Locate every uninfected red blood cell.
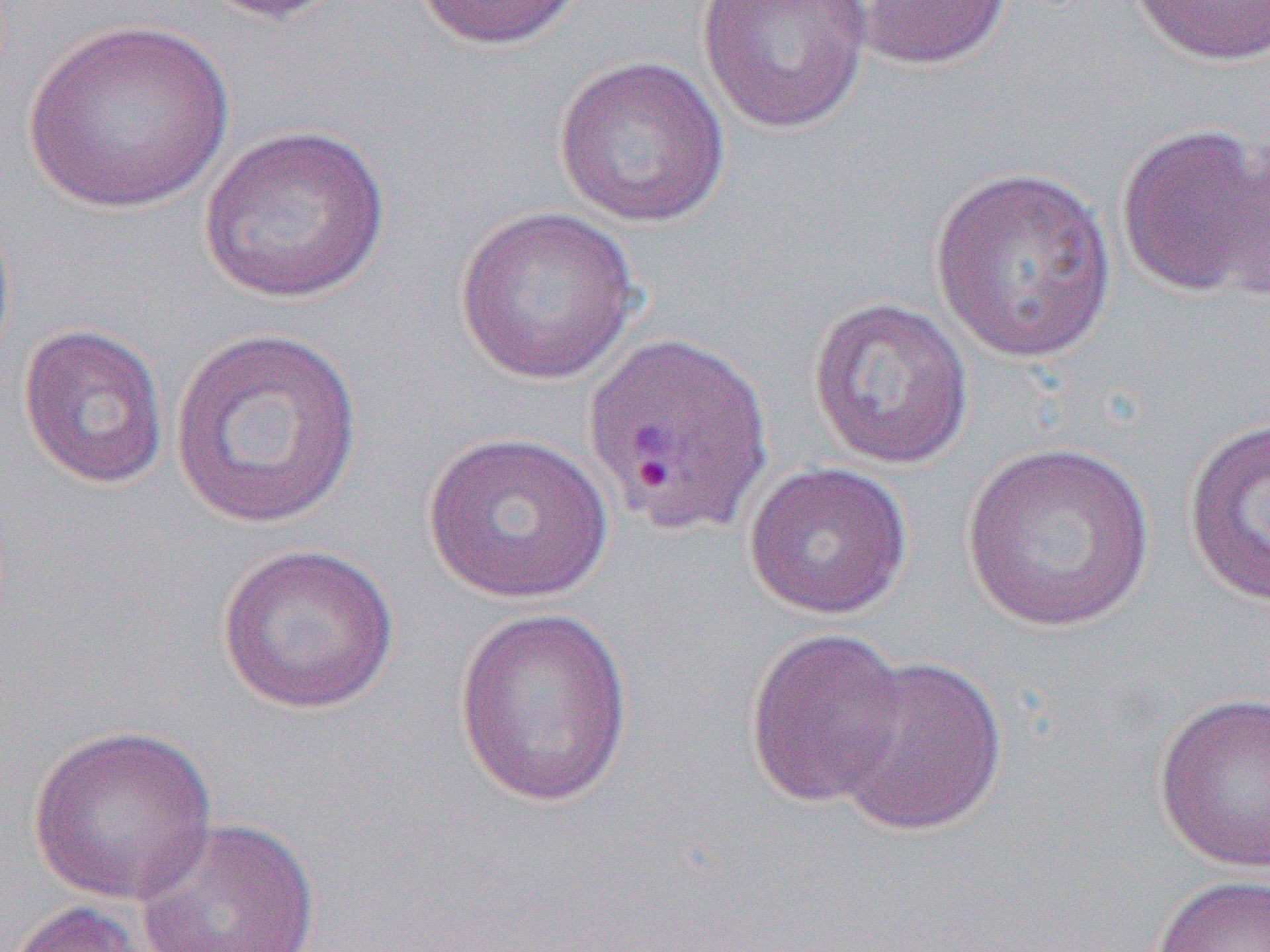
Approximate bounding boxes as (x1,y1)-(x2,y2) corner pairs in pixels.
Uninfected red blood cells: (198,0)-(350,24), (412,0)-(586,52), (696,0)-(873,135), (850,0)-(1013,71), (1129,0)-(1270,68), (22,19)-(237,216), (552,54)-(731,228), (198,124)-(391,304), (1115,124)-(1269,297), (1220,134)-(1269,305), (928,165)-(1119,364), (453,205)-(642,385), (0,209)-(16,373), (806,296)-(975,472), (18,322)-(169,489), (168,326)-(364,531), (1183,418)-(1270,608), (421,431)-(614,605), (961,440)-(1156,632), (742,461)-(913,621), (215,542)-(400,715), (453,606)-(634,807), (743,627)-(908,809), (834,654)-(1009,838), (1152,691)-(1270,875), (26,724)-(218,907), (133,816)-(321,952), (1148,872)-(1270,952), (5,899)-(156,952).

slide-level diagnosis = Plasmodium vivax
image size = 1270×952 pixels
magnification = 1000x
field of view = single
modality = light microscopy
preparation = thin blood smear